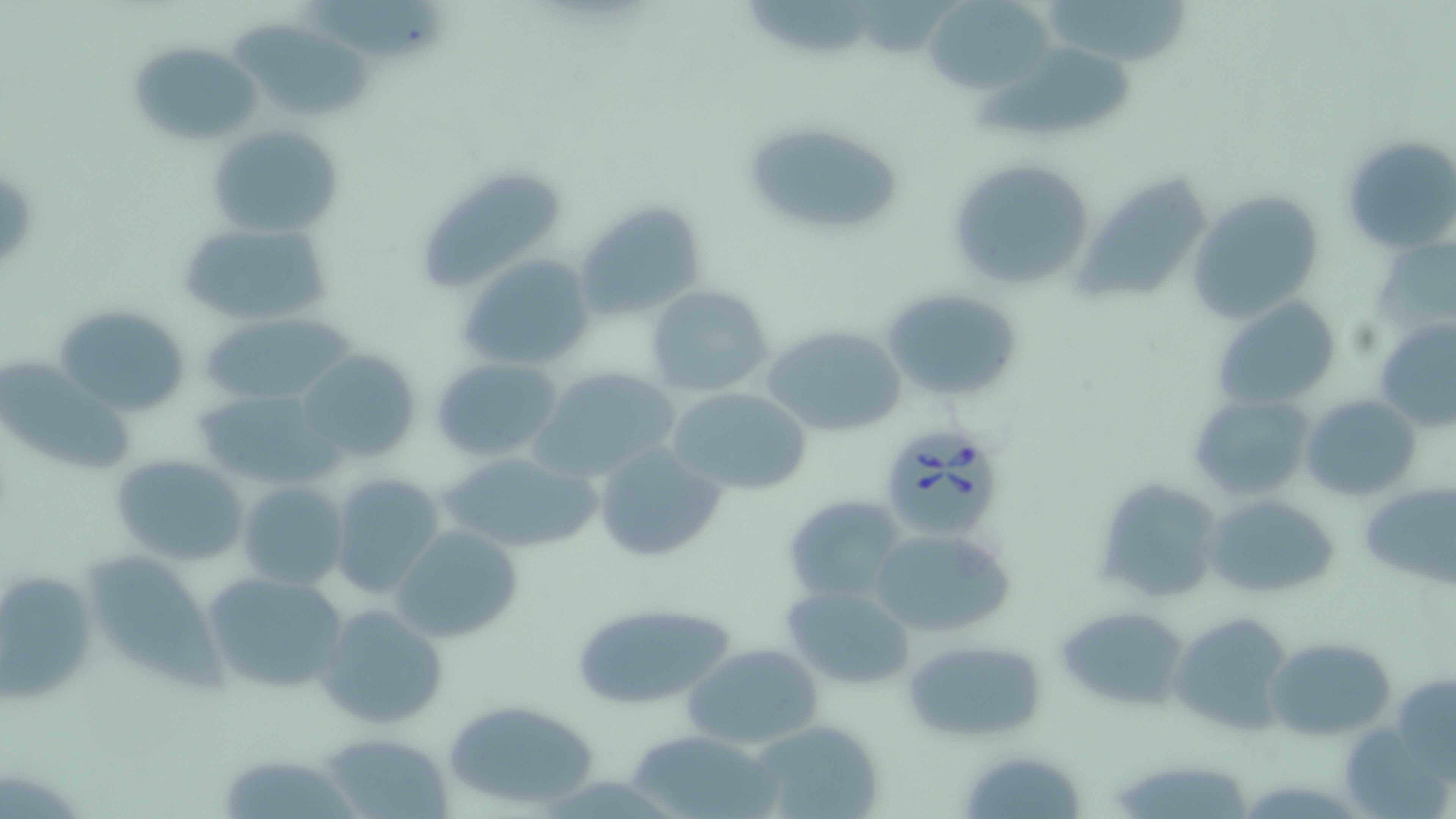 Approximate bounding boxes as (x1, y1, x2, y2) in pixels. Babesia divergens-infected red blood cell locations: (876, 423, 1001, 540). Uninfected red blood cell locations: (299, 0, 446, 60), (1040, 0, 1194, 65), (921, 1, 1057, 96), (743, 3, 878, 50), (229, 23, 375, 120), (126, 38, 261, 150), (975, 43, 1138, 140), (742, 121, 906, 237), (208, 124, 343, 237), (1340, 133, 1456, 255), (945, 157, 1099, 294), (425, 171, 562, 286), (1187, 189, 1328, 324), (575, 201, 708, 322), (175, 218, 337, 328), (1372, 234, 1455, 337), (458, 252, 598, 374), (646, 284, 776, 399), (879, 286, 1027, 404), (1212, 294, 1344, 413), (55, 305, 191, 416), (202, 312, 358, 407), (1375, 317, 1456, 436), (762, 323, 908, 436), (297, 348, 423, 464), (8, 353, 136, 476), (430, 357, 564, 462), (532, 366, 681, 482), (667, 386, 813, 496), (197, 389, 335, 489), (1190, 391, 1318, 501), (1299, 393, 1423, 501), (590, 441, 728, 563), (437, 450, 601, 555), (111, 454, 251, 565), (327, 471, 445, 598), (1090, 476, 1223, 605), (1358, 479, 1455, 591), (236, 480, 350, 591), (1201, 493, 1342, 600), (782, 494, 911, 604), (393, 525, 523, 644), (867, 527, 1015, 638), (92, 555, 232, 694), (0, 565, 97, 704), (201, 569, 351, 698), (780, 582, 916, 691), (315, 601, 451, 731), (569, 601, 738, 710), (1054, 605, 1193, 711), (1166, 611, 1292, 736), (1267, 636, 1395, 740), (901, 638, 1047, 743), (681, 643, 824, 750), (1390, 671, 1456, 778), (441, 697, 600, 811), (747, 719, 887, 819), (625, 728, 779, 819), (321, 732, 454, 818), (956, 747, 1089, 819), (221, 755, 357, 819), (1105, 756, 1261, 819). Slide-level diagnosis: Babesia divergens. Light microscopy. Single field of view. 1000x magnification. Image is 1456×819 pixels. Thin blood smear. May-Grünwald-Giemsa stain.